Outline each Plasmodium falciparum-infected red blood cell.
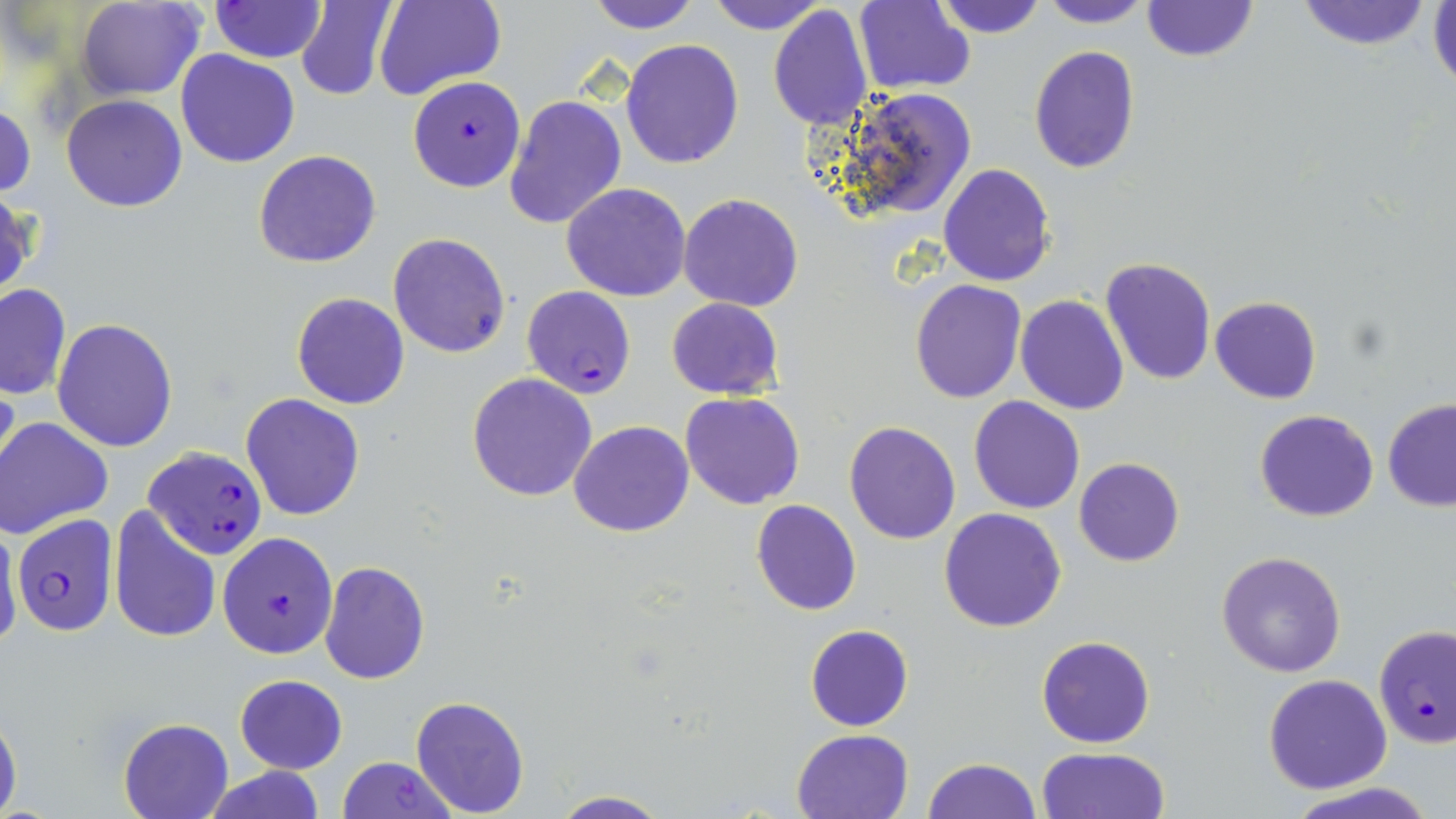

Approximate bounding boxes as (x1,y1)-(x2,y2) corner pairs in pixels.
Plasmodium falciparum-infected red blood cells: (407,75)-(525,192), (521,285)-(636,399), (144,446)-(268,560), (9,514)-(118,637), (217,531)-(337,659), (1374,624)-(1455,749), (336,757)-(458,819).

slide-level diagnosis = Plasmodium falciparum
stain = May-Grünwald-Giemsa
preparation = thin blood smear
uninfected red blood cell locations = approximate bounding boxes as (x1,y1)-(x2,y2) corner pairs in pixels: (76,0)-(205,99), (295,0)-(397,100), (375,0)-(505,103), (585,0)-(703,32), (706,0)-(827,34), (933,0)-(1047,39), (1039,0)-(1152,28), (1142,0)-(1257,61), (1294,0)-(1436,50), (855,1)-(976,95), (209,2)-(327,63), (1428,2)-(1456,98), (768,4)-(875,131), (621,40)-(745,169), (1029,45)-(1140,174), (176,49)-(301,167), (828,84)-(978,224), (61,94)-(187,211), (503,95)-(627,231), (1,102)-(36,200), (253,150)-(381,268), (937,164)-(1055,285), (561,182)-(691,301), (0,190)-(35,305), (679,193)-(803,312), (388,233)-(510,358), (1100,258)-(1217,387), (910,278)-(1027,402), (0,283)-(70,400), (292,293)-(410,410), (1015,294)-(1130,415), (1209,296)-(1322,405), (666,297)-(785,400), (52,317)-(179,452), (467,371)-(598,501), (0,374)-(24,493), (680,391)-(805,510), (240,392)-(366,520), (968,395)-(1085,514), (1383,399)-(1456,512), (1255,409)-(1379,522), (1,418)-(111,538), (568,421)-(694,536), (843,421)-(961,545), (1074,458)-(1184,567), (751,500)-(861,616), (939,507)-(1068,632), (109,508)-(222,644), (0,520)-(22,655), (1215,551)-(1347,678), (319,561)-(429,684), (805,624)-(913,731), (1036,636)-(1155,749), (234,673)-(348,774), (1263,673)-(1393,793), (411,692)-(533,814), (0,703)-(22,816), (119,719)-(232,818), (792,729)-(914,818), (1036,746)-(1170,819), (922,758)-(1040,819), (200,767)-(328,819), (1284,784)-(1441,819), (546,792)-(674,819)
magnification = 1000x
field of view = one of a larger specimen
modality = light microscopy
image size = 1456×819 pixels